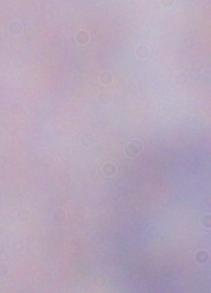
Summary:
  - Identification: trypanosome
  - Magnification: 1000x
  - Modality: photomicrograph